Classify this cell by malaria status.
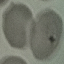

It is parasitized.

Cell patch, automatically extracted from a larger field of view and resized to 64 × 64 pixels. Thin blood smear. Giemsa-stained preparation. Acquired by smartphone through the microscope eyepiece.